Classify this cell by malaria status.
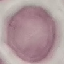
Uninfected.

Cell patch, automatically extracted from a larger field of view and resized to 64 × 64 pixels. Acquired by smartphone through the microscope eyepiece. Thin smear of blood. Giemsa stain.